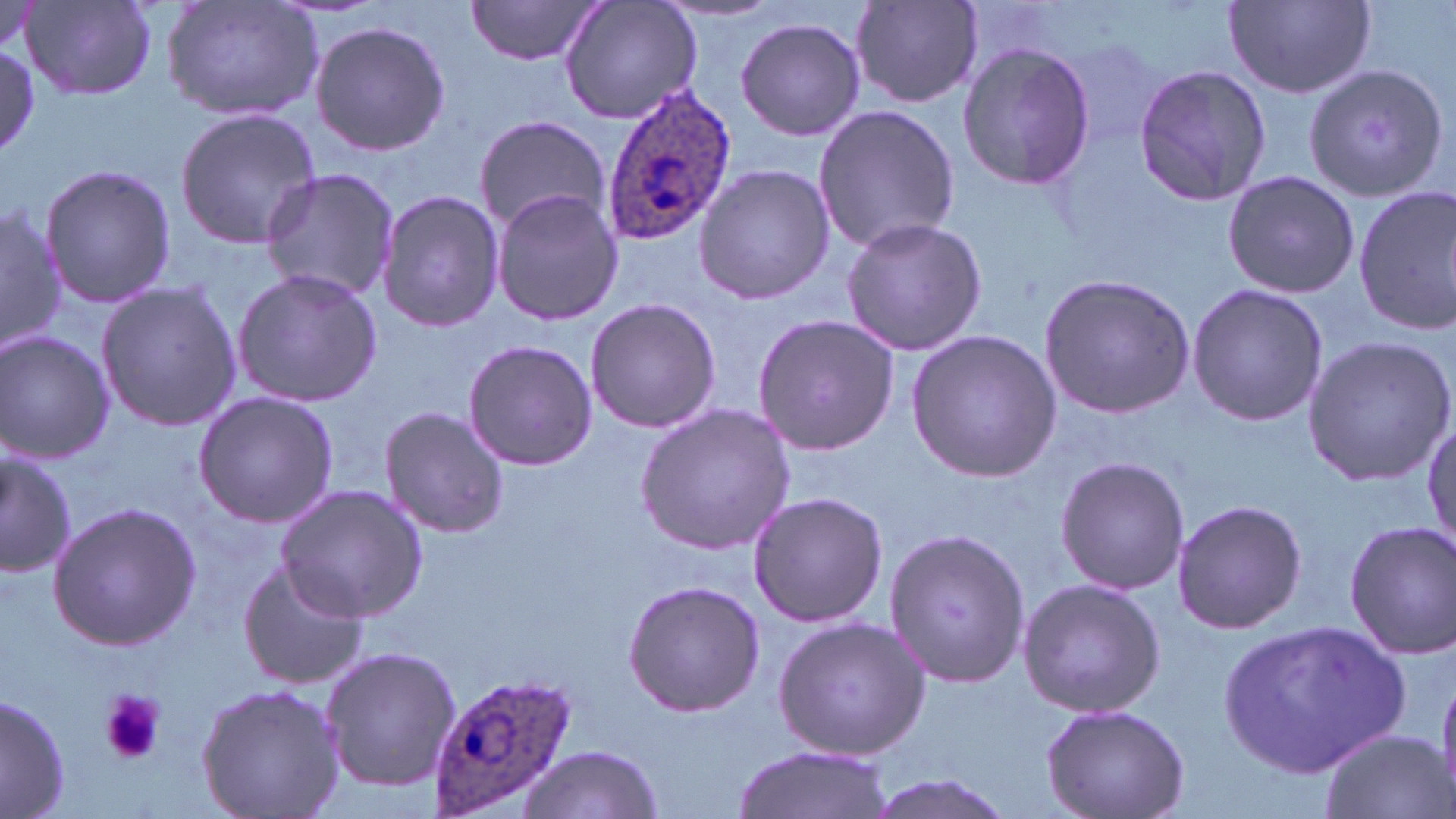

Approximate bounding boxes as [x1, y1, x2, y2] in pixels. Platelet locations: [99, 688, 164, 766]. Plasmodium ovale-infected red blood cell locations: [598, 83, 738, 243], [427, 670, 579, 815]. Uninfected red blood cell locations: [463, 0, 608, 67], [557, 0, 704, 126], [1223, 0, 1377, 98], [20, 1, 157, 101], [161, 1, 323, 122], [850, 1, 985, 109], [734, 17, 866, 140], [309, 19, 449, 157], [0, 43, 40, 159], [957, 43, 1097, 189], [1133, 62, 1273, 207], [1305, 63, 1451, 205], [812, 104, 960, 255], [174, 108, 321, 251], [472, 114, 610, 236], [39, 163, 175, 308], [693, 163, 835, 305], [260, 168, 401, 304], [1221, 170, 1360, 298], [1353, 186, 1456, 335], [490, 188, 624, 325], [376, 192, 505, 334], [0, 199, 65, 356], [839, 216, 988, 356], [231, 267, 382, 408], [1037, 273, 1196, 419], [96, 280, 242, 431], [1186, 282, 1328, 427], [583, 296, 722, 433], [753, 312, 899, 457], [906, 329, 1064, 484], [0, 331, 115, 464], [1300, 333, 1455, 487], [462, 338, 598, 470], [193, 391, 338, 526], [635, 402, 798, 554], [379, 407, 511, 538], [1423, 420, 1455, 559], [0, 448, 76, 574], [1054, 456, 1189, 596], [276, 487, 426, 621], [746, 490, 887, 628], [1171, 497, 1307, 636], [47, 502, 200, 650], [1344, 521, 1455, 658], [882, 525, 1030, 690], [235, 559, 369, 690], [1016, 577, 1167, 720], [623, 580, 766, 718], [772, 617, 930, 762], [1223, 620, 1415, 776], [321, 645, 462, 790], [195, 683, 344, 819], [1, 692, 71, 819], [1041, 701, 1192, 819], [1318, 729, 1451, 819], [731, 740, 891, 819], [517, 745, 664, 818], [861, 773, 1013, 819]. Slide-level diagnosis: Plasmodium ovale. 1000x magnification. Light microscopy. Single field of view. Thin blood smear. May-Grünwald-Giemsa-stained preparation. Image is 1456×819 pixels.